State the blood parasite species.
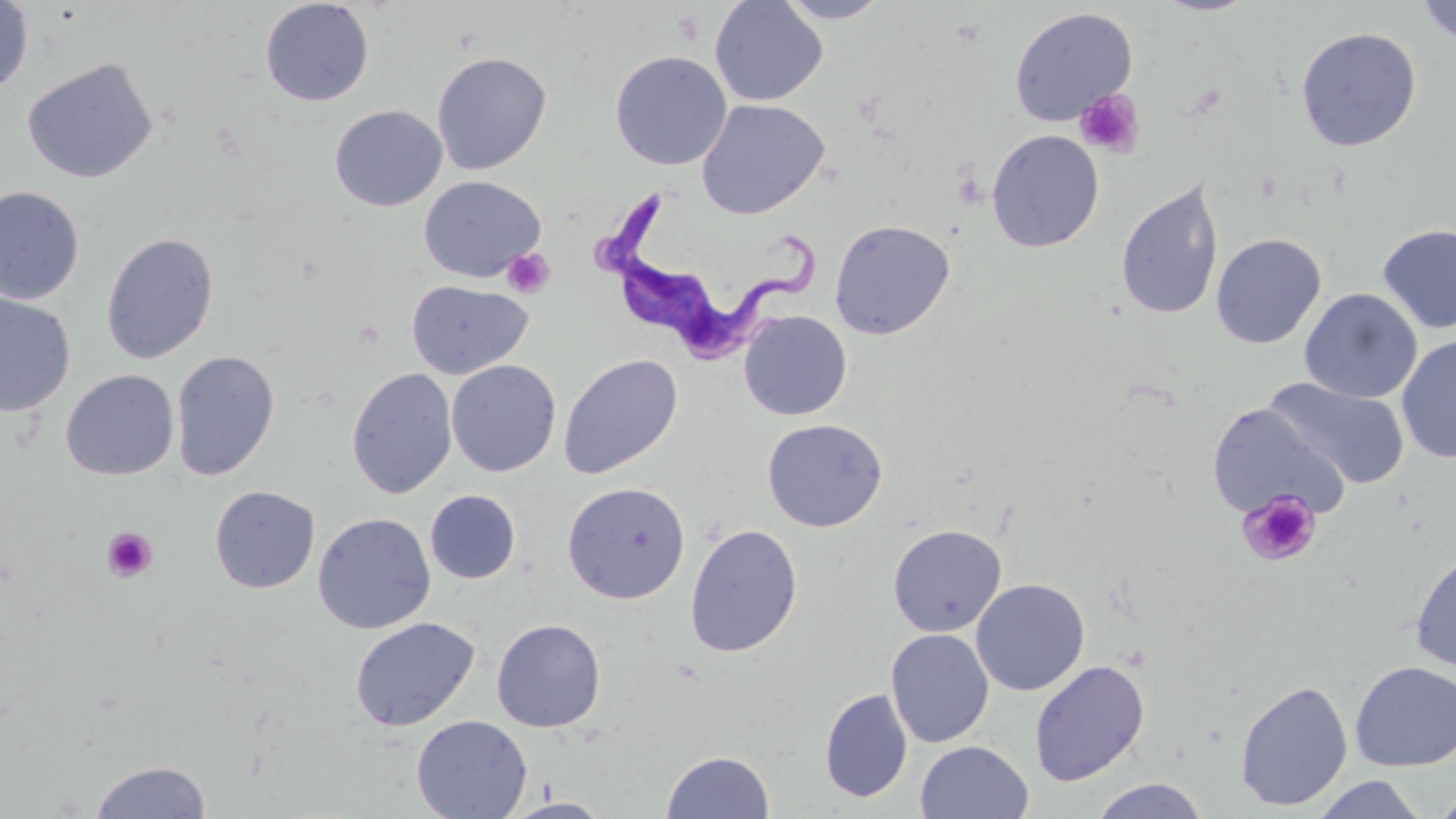

Trypanosoma brucei.

uninfected_red_blood_cell_locations: 'approximate bounding boxes as named x1/y1/x2/y2 corners in pixels: (x1=709, y1=0, x2=829, y2=106), (x1=776, y1=0, x2=891, y2=23), (x1=1155, y1=0, x2=1258, y2=16), (x1=1416, y1=0, x2=1456, y2=44), (x1=0, y1=1, x2=33, y2=96), (x1=260, y1=1, x2=374, y2=106), (x1=1009, y1=6, x2=1138, y2=126), (x1=1295, y1=26, x2=1422, y2=152), (x1=609, y1=50, x2=732, y2=171), (x1=431, y1=51, x2=552, y2=176), (x1=21, y1=56, x2=158, y2=184), (x1=696, y1=99, x2=829, y2=219), (x1=330, y1=105, x2=447, y2=211), (x1=986, y1=129, x2=1105, y2=253), (x1=1115, y1=174, x2=1225, y2=322), (x1=418, y1=175, x2=545, y2=282), (x1=0, y1=186, x2=84, y2=305), (x1=829, y1=218, x2=956, y2=340), (x1=1376, y1=224, x2=1456, y2=334), (x1=101, y1=231, x2=219, y2=364), (x1=1210, y1=233, x2=1326, y2=349), (x1=406, y1=280, x2=532, y2=379), (x1=1300, y1=288, x2=1422, y2=403), (x1=0, y1=292, x2=76, y2=417), (x1=738, y1=310, x2=852, y2=420), (x1=1397, y1=334, x2=1456, y2=464), (x1=170, y1=349, x2=280, y2=481), (x1=558, y1=353, x2=683, y2=480), (x1=446, y1=360, x2=561, y2=477), (x1=346, y1=367, x2=458, y2=499), (x1=61, y1=369, x2=179, y2=481), (x1=1264, y1=377, x2=1411, y2=491), (x1=1207, y1=402, x2=1348, y2=522), (x1=762, y1=418, x2=888, y2=532), (x1=562, y1=481, x2=691, y2=604), (x1=209, y1=485, x2=320, y2=594), (x1=425, y1=489, x2=521, y2=584), (x1=312, y1=513, x2=435, y2=634), (x1=685, y1=523, x2=803, y2=658), (x1=887, y1=523, x2=1007, y2=637), (x1=1410, y1=549, x2=1456, y2=672), (x1=971, y1=578, x2=1090, y2=696), (x1=350, y1=617, x2=480, y2=732), (x1=492, y1=619, x2=606, y2=732), (x1=886, y1=628, x2=995, y2=748), (x1=1029, y1=659, x2=1150, y2=786), (x1=1350, y1=661, x2=1456, y2=771), (x1=1234, y1=679, x2=1353, y2=811), (x1=820, y1=687, x2=913, y2=803), (x1=412, y1=715, x2=532, y2=819), (x1=916, y1=741, x2=1033, y2=818), (x1=661, y1=750, x2=774, y2=818), (x1=89, y1=759, x2=212, y2=819), (x1=1310, y1=775, x2=1428, y2=818), (x1=1089, y1=778, x2=1212, y2=818), (x1=1431, y1=789, x2=1456, y2=818), (x1=502, y1=796, x2=613, y2=818)'
magnification: 1000x
platelet_locations: 'approximate bounding boxes as named x1/y1/x2/y2 corners in pixels: (x1=1074, y1=89, x2=1144, y2=158), (x1=501, y1=248, x2=555, y2=299), (x1=1238, y1=491, x2=1321, y2=567), (x1=101, y1=527, x2=158, y2=583)'
preparation: thin blood film
image_size: 1456×819 pixels
trypanosoma_brucei_locations: 'approximate bounding boxes as named x1/y1/x2/y2 corners in pixels: (x1=595, y1=187, x2=819, y2=361)'
stain: May-Grünwald-Giemsa
modality: optical microscopy
field_of_view: single